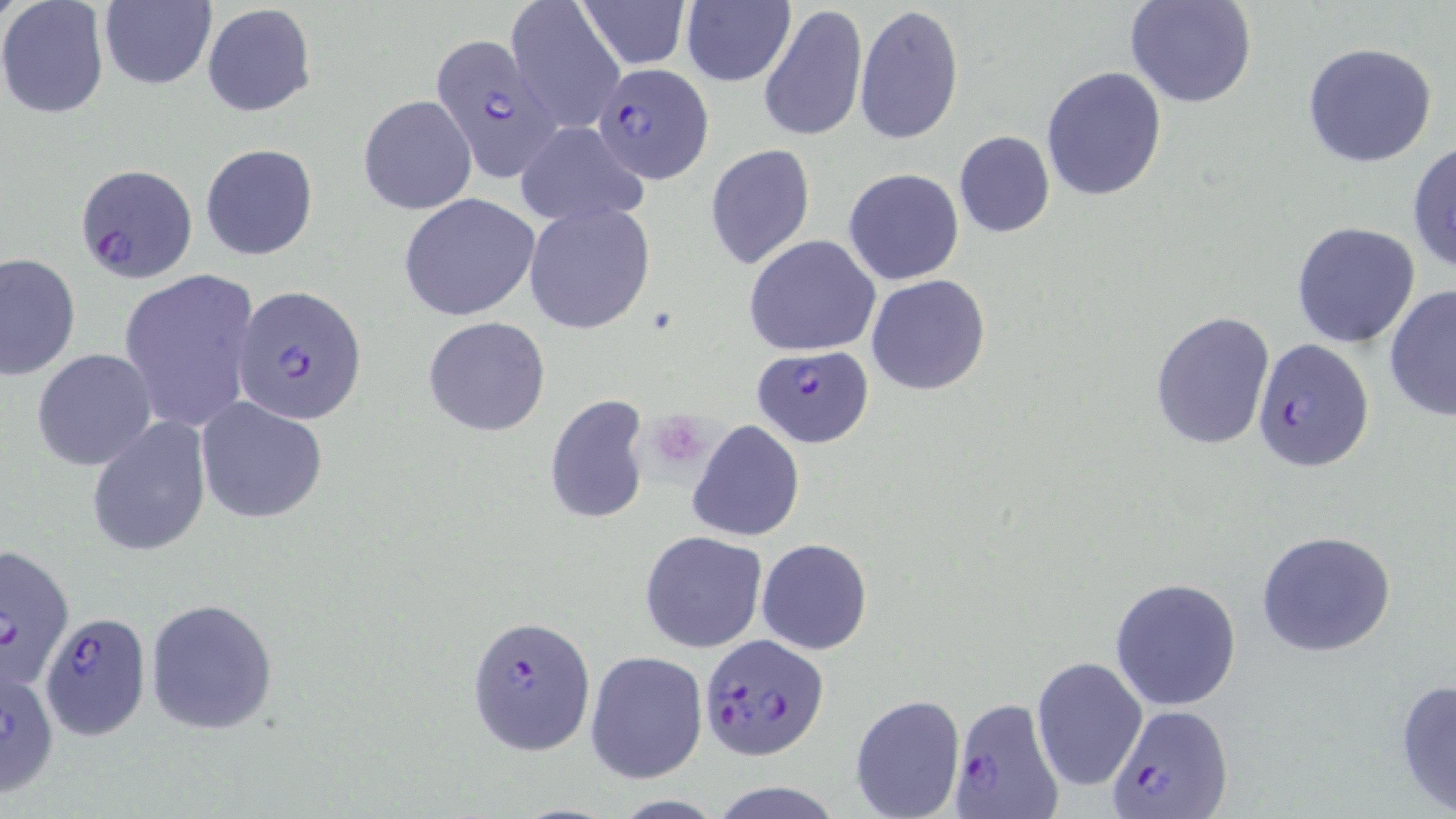
Summary:
  - Coordinate format: approximate bounding boxes as [x1, y1, x2, y2] in pixels
  - Platelet locations: [650, 414, 715, 472]
  - Uninfected red blood cell locations: [0, 0, 110, 120], [574, 0, 691, 69], [1124, 0, 1258, 109], [97, 1, 217, 90], [506, 1, 626, 132], [681, 1, 794, 87], [758, 2, 868, 144], [202, 3, 317, 118], [854, 3, 962, 147], [1300, 42, 1439, 168], [1041, 66, 1167, 200], [358, 94, 477, 214], [515, 121, 650, 229], [953, 131, 1056, 238], [1407, 140, 1455, 272], [200, 142, 320, 262], [704, 143, 816, 270], [844, 168, 964, 286], [398, 193, 543, 322], [522, 202, 656, 334], [1291, 222, 1421, 348], [743, 235, 881, 356], [0, 252, 81, 382], [117, 268, 262, 433], [866, 275, 990, 394], [1383, 283, 1456, 421], [1150, 310, 1275, 450], [423, 315, 550, 436], [32, 348, 157, 470], [543, 394, 652, 525], [197, 399, 328, 522], [86, 416, 212, 558], [687, 419, 805, 542], [1256, 530, 1396, 658], [639, 531, 767, 652], [756, 538, 873, 654], [1109, 577, 1241, 711], [146, 598, 277, 734], [585, 650, 708, 782], [1030, 654, 1147, 793], [1394, 678, 1456, 815], [848, 693, 963, 818], [710, 781, 841, 818], [608, 795, 728, 818]
  - Plasmodium falciparum-infected red blood cell locations: [427, 33, 563, 185], [591, 63, 714, 183], [73, 164, 196, 283], [233, 288, 367, 423], [1252, 337, 1375, 473], [750, 345, 874, 448], [0, 541, 75, 689], [42, 614, 150, 739], [466, 614, 596, 757], [699, 631, 830, 763], [1, 661, 60, 797], [950, 698, 1067, 818], [1106, 702, 1231, 819]
  - Slide-level diagnosis: Plasmodium falciparum
  - Image size: 1456×819 pixels
  - Stain: May-Grünwald-Giemsa
  - Modality: light microscopy
  - Preparation: thin blood smear
  - Field of view: single
  - Magnification: 1000x